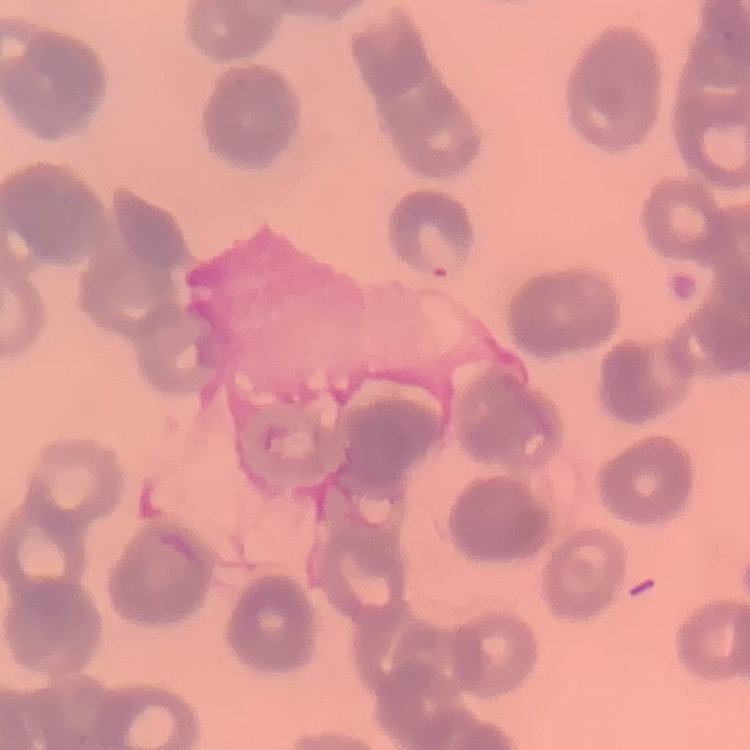

red blood cell morphology = rouleaux formation
stain = Field's or Giemsa
preparation = thin peripheral smear
image type = one tile cut from a larger photomicrograph